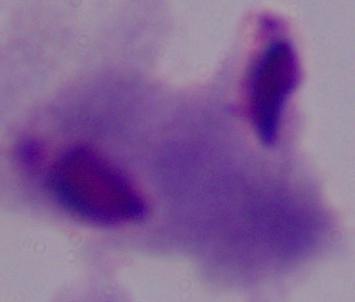

Summary:
  - Identification: trichomonad
  - Magnification: 1000x
  - Modality: photomicrograph